Report the malaria status of this cell.
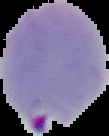

It is parasitized.

Cell region segmented out of the field of view; the surrounding area is masked to black. Image is 109×136 pixels. From a thin blood smear.